Assess this cell for malaria.
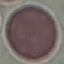

It is uninfected.

Giemsa stain. Thin blood film. Cell patch, automatically extracted from a larger field of view and resized to 64 × 64 pixels. Acquired by smartphone through the microscope eyepiece.